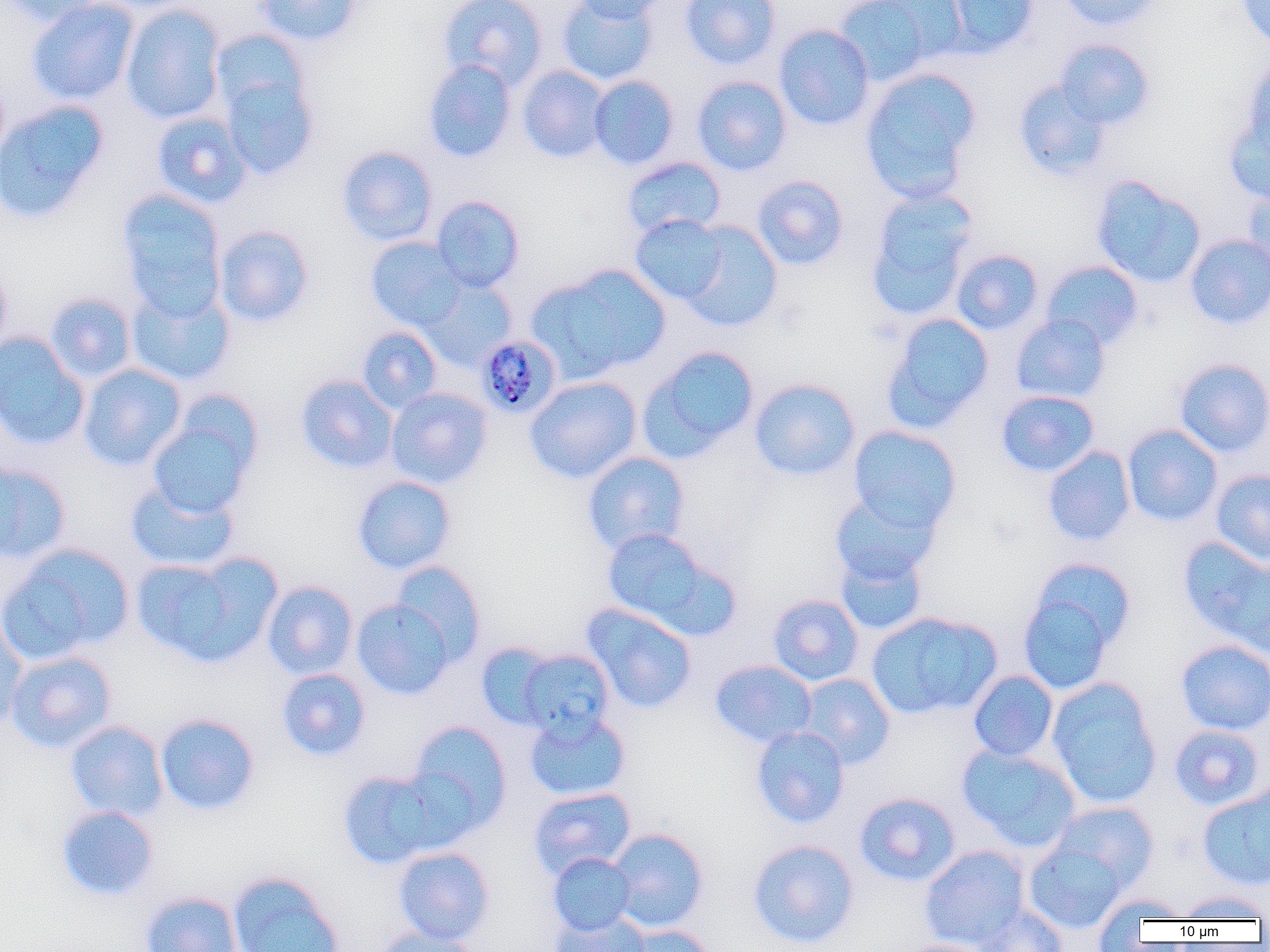

Summary:
  - Coordinate format: approximate bounding boxes as [x1, y1, x2, y2] in pixels
  - Plasmodium malariae-infected red blood cell locations: [476, 334, 562, 420]
  - Uninfected red blood cell locations: [0, 0, 105, 26], [26, 0, 139, 105], [255, 0, 363, 46], [437, 0, 548, 91], [557, 0, 658, 85], [569, 0, 671, 22], [680, 0, 781, 70], [833, 0, 943, 84], [943, 0, 1041, 57], [1057, 0, 1166, 31], [1235, 0, 1270, 50], [120, 3, 226, 125], [773, 24, 875, 131], [209, 28, 311, 123], [1054, 39, 1155, 130], [1240, 56, 1270, 160], [422, 59, 517, 163], [517, 65, 611, 163], [859, 68, 982, 203], [218, 72, 319, 180], [588, 75, 680, 170], [691, 75, 792, 176], [1013, 77, 1114, 181], [0, 100, 109, 224], [150, 111, 252, 208], [1224, 118, 1270, 205], [337, 145, 438, 246], [620, 156, 726, 239], [751, 175, 849, 270], [1090, 175, 1206, 288], [1243, 181, 1270, 275], [865, 187, 978, 320], [116, 188, 226, 311], [431, 196, 525, 293], [629, 214, 730, 304], [676, 220, 784, 331], [213, 225, 315, 328], [1184, 234, 1270, 330], [365, 237, 467, 332], [951, 249, 1044, 335], [0, 259, 13, 355], [1039, 260, 1145, 352], [529, 265, 671, 383], [418, 276, 517, 371], [126, 282, 236, 386], [44, 291, 137, 384], [882, 312, 994, 431], [1010, 313, 1112, 404], [356, 326, 443, 414], [0, 331, 89, 451], [638, 344, 760, 462], [1173, 357, 1270, 458], [79, 363, 187, 471], [295, 374, 398, 474], [524, 376, 642, 484], [748, 378, 861, 482], [386, 388, 493, 489], [995, 390, 1099, 478], [146, 400, 261, 520], [1122, 424, 1223, 527], [846, 425, 962, 534], [1042, 445, 1136, 547], [582, 451, 691, 556], [0, 463, 69, 565], [1210, 469, 1270, 566], [351, 475, 457, 574], [125, 479, 239, 573], [829, 491, 940, 587], [600, 528, 735, 638], [1178, 537, 1270, 649], [2, 543, 134, 663], [834, 545, 929, 636], [130, 553, 278, 667], [391, 560, 487, 664], [1017, 560, 1133, 693], [261, 580, 358, 680], [767, 594, 864, 686], [352, 598, 455, 699], [581, 604, 698, 713], [0, 611, 29, 734], [866, 611, 1002, 720], [1175, 639, 1270, 735], [475, 641, 559, 730], [517, 649, 615, 737], [4, 650, 118, 753], [710, 659, 817, 748], [276, 668, 371, 762], [968, 670, 1059, 762], [795, 673, 895, 769], [1046, 677, 1163, 809], [524, 710, 631, 802], [154, 713, 261, 815], [65, 720, 169, 822], [406, 720, 513, 838], [1168, 724, 1266, 811], [751, 725, 850, 829], [957, 744, 1082, 852], [336, 769, 447, 869], [1197, 785, 1270, 892], [528, 787, 636, 880], [853, 792, 961, 887], [1049, 801, 1158, 893], [55, 804, 160, 901], [606, 828, 710, 933], [747, 839, 860, 949], [1024, 839, 1129, 934], [919, 844, 1030, 950], [393, 846, 495, 945], [548, 853, 636, 936], [227, 871, 345, 952], [138, 890, 243, 952], [1176, 890, 1269, 922], [1092, 892, 1191, 939], [972, 904, 1069, 952], [549, 909, 651, 952], [619, 925, 715, 952], [370, 928, 485, 952], [895, 939, 1000, 952]
  - Slide-level diagnosis: Plasmodium malariae
  - Preparation: thin blood film
  - Magnification: 1000x
  - Modality: optical microscopy
  - Image size: 1270×952 pixels
  - Field of view: one of a larger specimen